Report the malaria status of this cell.
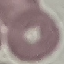

Uninfected.

capture = smartphone camera at the microscope eyepiece
image type = automatically extracted cell patch, resized to 64 × 64 pixels
preparation = thin smear
stain = Giemsa